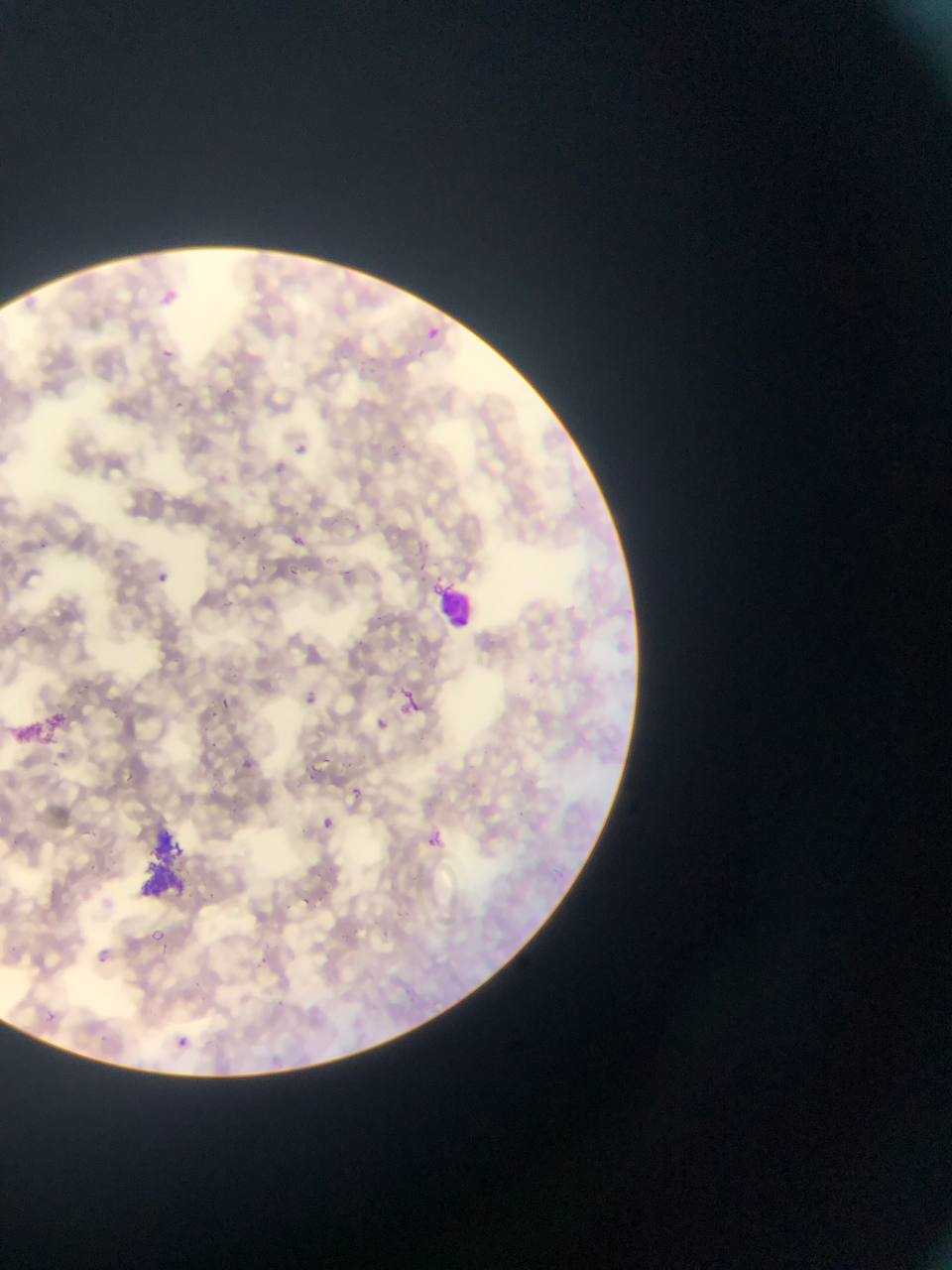

{
  "preparation": "thin blood smear",
  "capture": "mobile-phone photograph through a microscope",
  "country": "Ghana",
  "leukocyte_locations": "approximate bounding boxes as [left, top, right, bottom] in pixels: [435, 577, 471, 628]",
  "image_size": "952×1270 pixels",
  "field_of_view": "single",
  "plasmodium_parasite_locations": "approximate bounding boxes as [left, top, right, bottom] in pixels: [160, 293, 181, 306], [428, 325, 446, 346], [156, 342, 173, 359], [168, 397, 183, 418], [293, 438, 310, 452], [264, 457, 288, 475], [285, 504, 300, 520], [239, 526, 262, 545], [294, 535, 305, 546], [254, 560, 273, 574], [155, 563, 172, 580], [288, 563, 305, 575], [396, 683, 425, 730], [303, 687, 318, 710], [216, 689, 245, 714], [373, 713, 390, 737], [240, 754, 257, 766], [323, 754, 332, 763], [343, 783, 364, 806], [315, 815, 329, 836], [420, 828, 448, 849], [148, 930, 167, 943], [85, 944, 123, 976], [41, 1004, 66, 1021], [177, 1035, 197, 1056]"
}